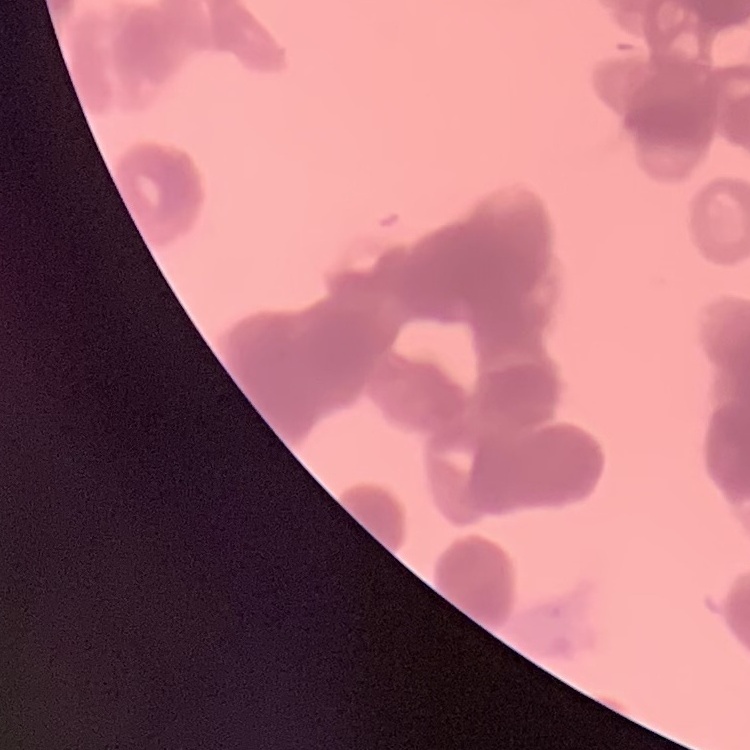
erythrocyte morphology = rouleaux formation
preparation = thin peripheral smear
image type = square crop of a larger photomicrograph
stain = Field's or Giemsa